State the blood parasite species.
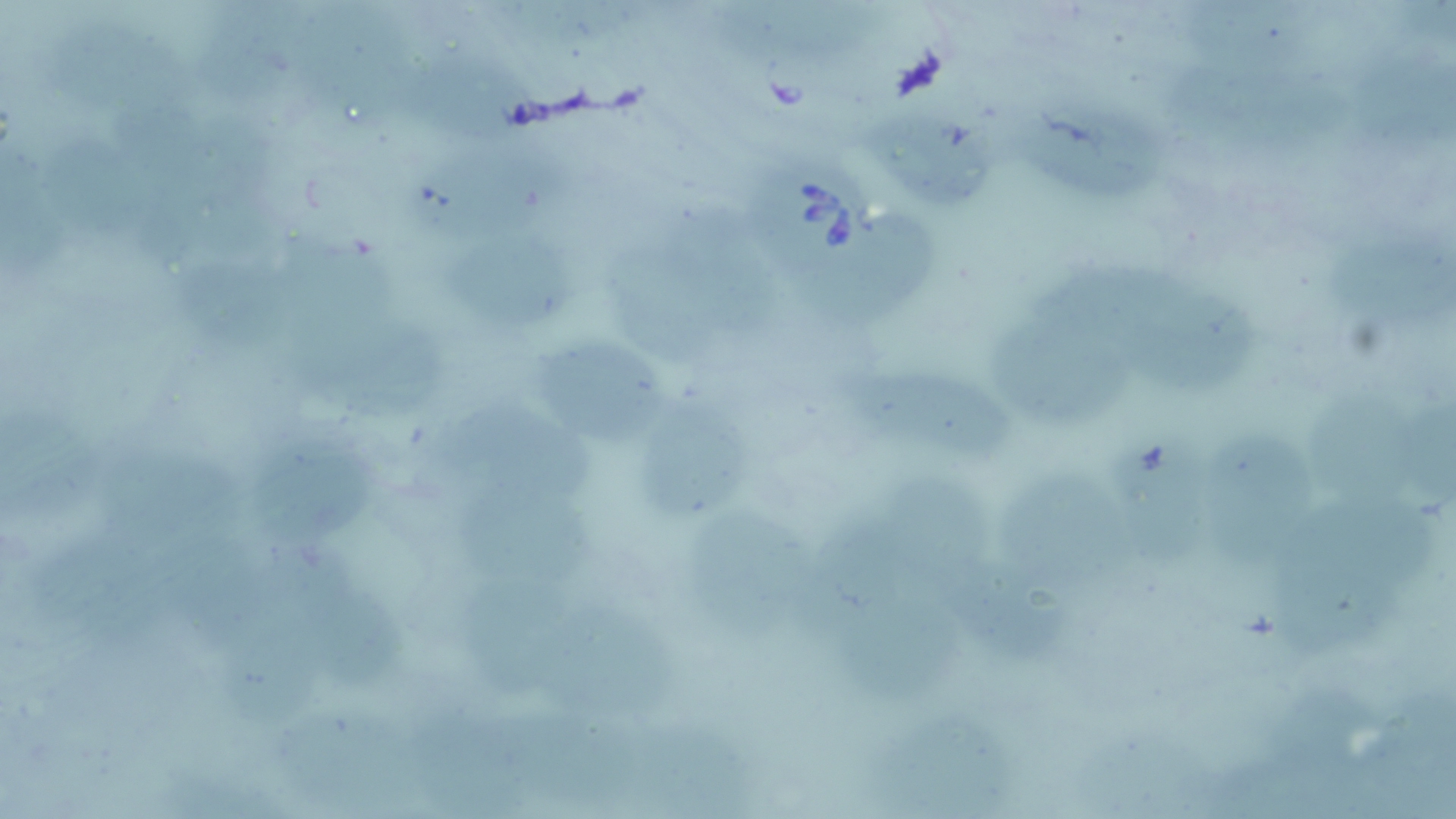

Babesia divergens.

Approximate bounding boxes as [x1, y1, x2, y2] in pixels. Babesia divergens-infected red blood cell locations: [742, 151, 882, 281]. Uninfected red blood cell locations: [201, 0, 310, 110], [712, 0, 904, 65], [283, 3, 423, 125], [34, 13, 204, 116], [1352, 43, 1456, 149], [392, 48, 554, 138], [1007, 85, 1186, 206], [861, 104, 995, 207], [36, 126, 152, 246], [390, 139, 595, 242], [666, 205, 792, 341], [796, 215, 946, 328], [1327, 223, 1456, 341], [428, 227, 589, 328], [602, 231, 736, 367], [167, 249, 332, 357], [1125, 273, 1277, 401], [293, 296, 450, 429], [989, 314, 1130, 434], [533, 332, 677, 446], [836, 363, 1022, 462], [630, 386, 761, 531], [1302, 390, 1422, 513], [433, 403, 601, 507], [1, 405, 111, 527], [242, 424, 377, 556], [1112, 429, 1229, 576], [1210, 430, 1318, 577], [91, 435, 246, 545], [996, 468, 1140, 598], [451, 473, 599, 594], [1272, 498, 1434, 662], [683, 501, 812, 645], [38, 531, 174, 662], [169, 534, 298, 655], [279, 549, 417, 694], [943, 556, 1075, 666], [473, 579, 584, 702], [216, 597, 330, 732], [833, 600, 968, 706], [533, 602, 688, 724], [268, 693, 437, 816], [869, 710, 1016, 818]. Single field of view. May-Grünwald-Giemsa stain. Image is 1456×819 pixels. Captured at 1000x magnification. Optical microscopy. Thin blood smear.